Classify this cell by malaria status.
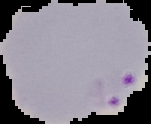

It is parasitized.

preparation = thin blood smear
image type = segmented cell region with the area outside set to black
image size = 151×124 pixels